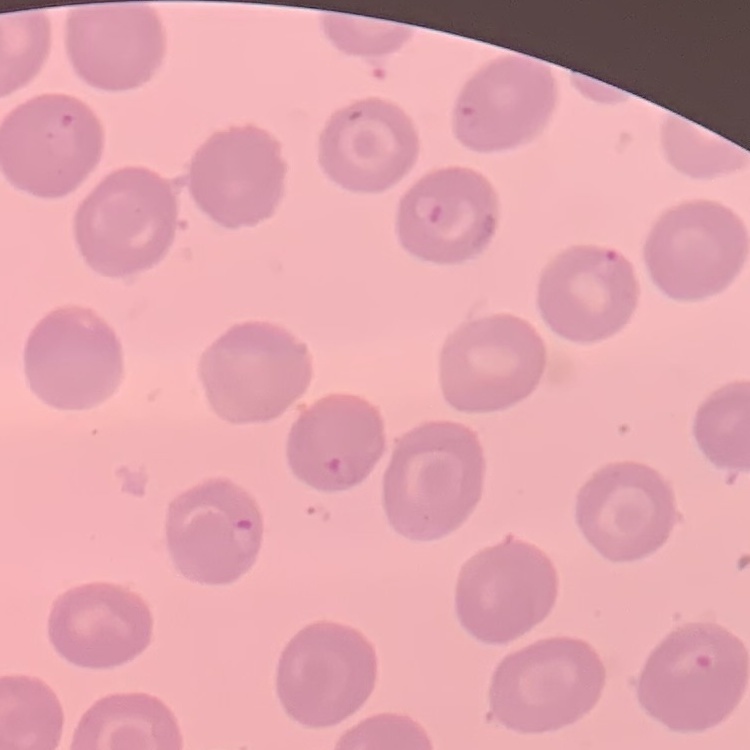
{
  "red_blood_cell_morphology": "no rouleaux formation",
  "preparation": "thin blood film",
  "stain": "Field's or Giemsa",
  "image_type": "square crop of a larger photomicrograph"
}